Classify this cell by malaria status.
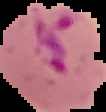
It is parasitized.

Image is 106×112 pixels. Cell region segmented out of the field of view; the surrounding area is masked to black. From a thin blood smear.